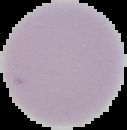
Summary:
  - Image type: cell region segmented out of the field of view; surrounding area masked to black
  - Malaria status: uninfected
  - Preparation: thin blood smear
  - Image size: 127×130 pixels